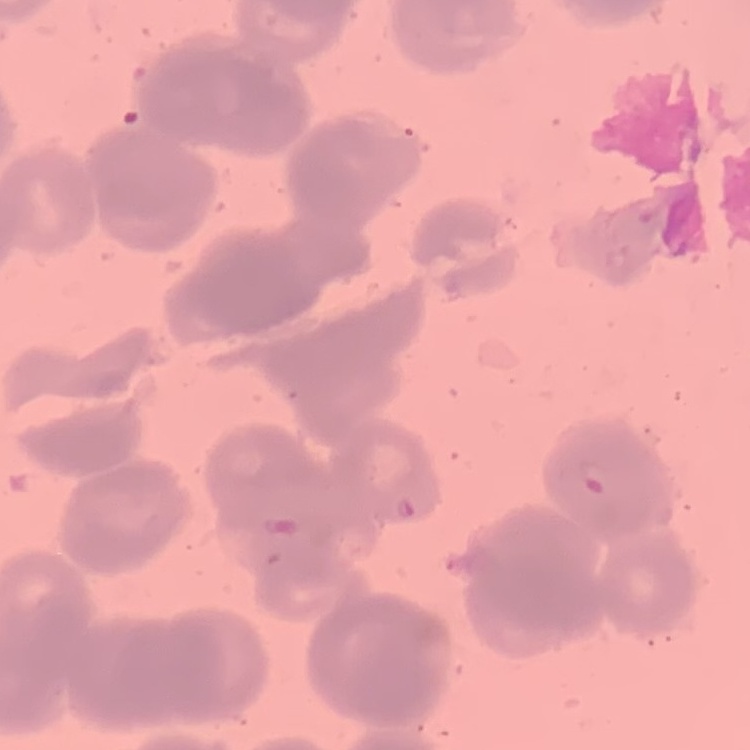
erythrocyte morphology = rouleaux formation
preparation = thin blood film
stain = Field's or Giemsa
image type = square crop of a larger photomicrograph